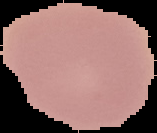

Summary:
  - Image size: 157×133 pixels
  - Result: no Plasmodium parasites detected
  - Image type: segmented cell region with the area outside set to black
  - Preparation: thin blood film